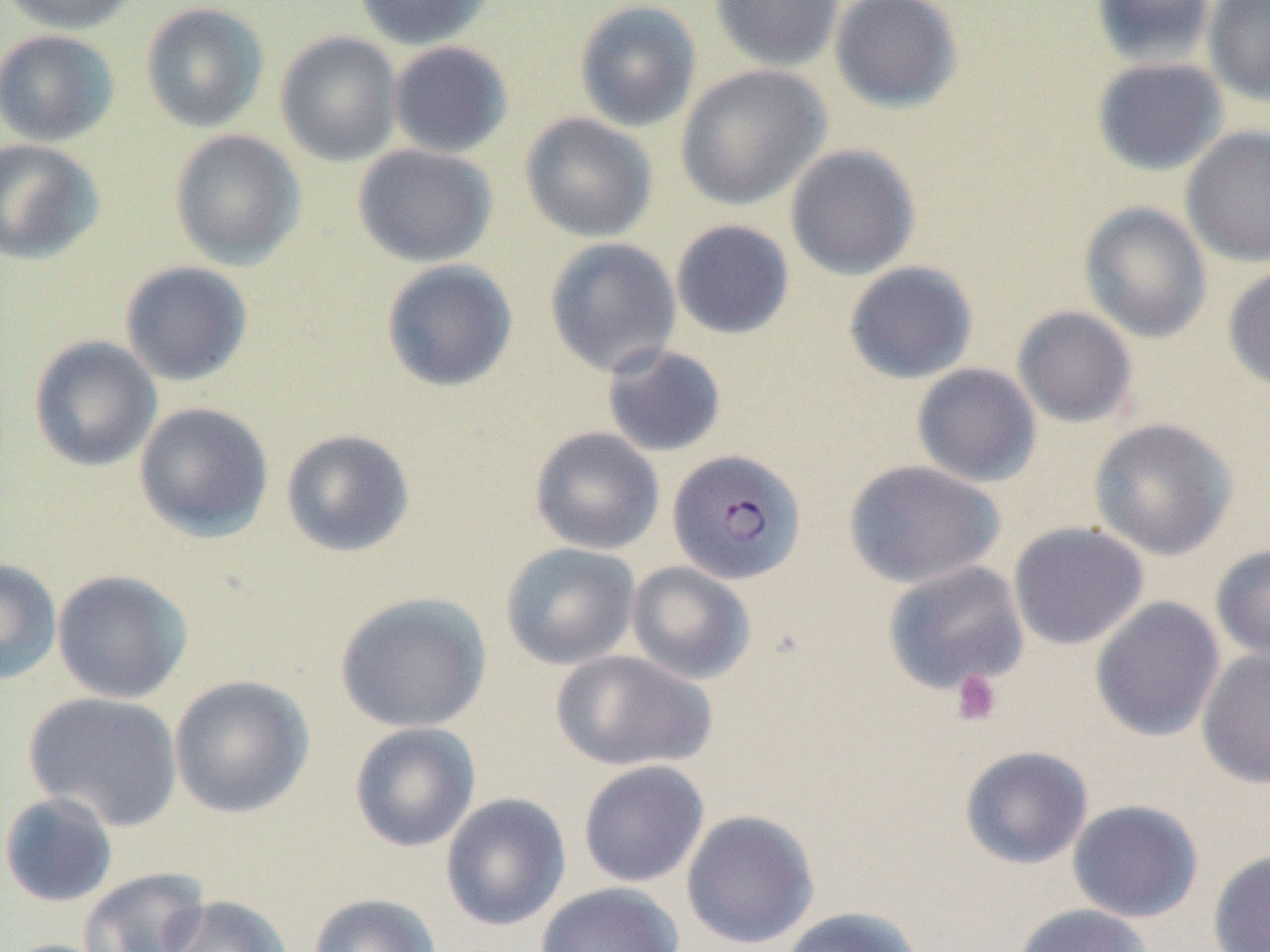
Summary:
  - Coordinate format: approximate bounding boxes as [x1, y1, x2, y2] in pixels
  - Uninfected red blood cell locations: [2, 0, 141, 35], [353, 0, 495, 50], [709, 0, 844, 72], [828, 0, 964, 113], [1091, 0, 1216, 67], [1202, 0, 1270, 105], [140, 1, 269, 133], [574, 1, 702, 132], [0, 29, 119, 147], [275, 30, 402, 167], [388, 40, 513, 159], [1091, 56, 1229, 176], [675, 65, 831, 210], [519, 112, 658, 243], [1180, 124, 1270, 268], [168, 129, 306, 270], [0, 138, 105, 265], [352, 144, 498, 268], [785, 144, 921, 281], [1078, 201, 1212, 343], [670, 219, 795, 340], [543, 237, 682, 377], [380, 259, 518, 392], [120, 260, 253, 386], [843, 261, 978, 384], [1222, 261, 1270, 393], [1012, 306, 1137, 428], [28, 335, 162, 472], [601, 343, 727, 458], [911, 362, 1042, 487], [133, 401, 274, 541], [1089, 418, 1238, 560], [529, 426, 664, 555], [280, 428, 415, 558], [843, 459, 1005, 589], [1008, 521, 1149, 650], [500, 542, 640, 669], [1210, 543, 1270, 664], [0, 557, 62, 686], [882, 560, 1029, 694], [626, 561, 756, 685], [51, 569, 193, 704], [334, 591, 492, 733], [1090, 597, 1225, 742], [1197, 648, 1270, 789], [552, 649, 717, 773], [168, 674, 315, 819], [23, 691, 183, 831], [349, 721, 481, 853], [959, 745, 1093, 870], [578, 760, 710, 888], [0, 791, 118, 908], [440, 792, 571, 931], [1067, 799, 1204, 923], [681, 810, 820, 950], [1207, 849, 1270, 952], [77, 867, 211, 952], [535, 881, 685, 952], [307, 893, 441, 952], [159, 894, 292, 952], [1012, 903, 1155, 952], [777, 906, 924, 952], [2, 938, 120, 952]
  - Plasmodium falciparum-infected red blood cell locations: [667, 448, 806, 585]
  - Platelet locations: [950, 669, 1002, 726]
  - Slide-level diagnosis: Plasmodium falciparum
  - Magnification: 1000x
  - Field of view: one of a larger specimen
  - Preparation: thin blood smear
  - Modality: light microscopy
  - Image size: 1270×952 pixels
  - Stain: May-Grünwald-Giemsa